Point out each Plasmodium parasite.
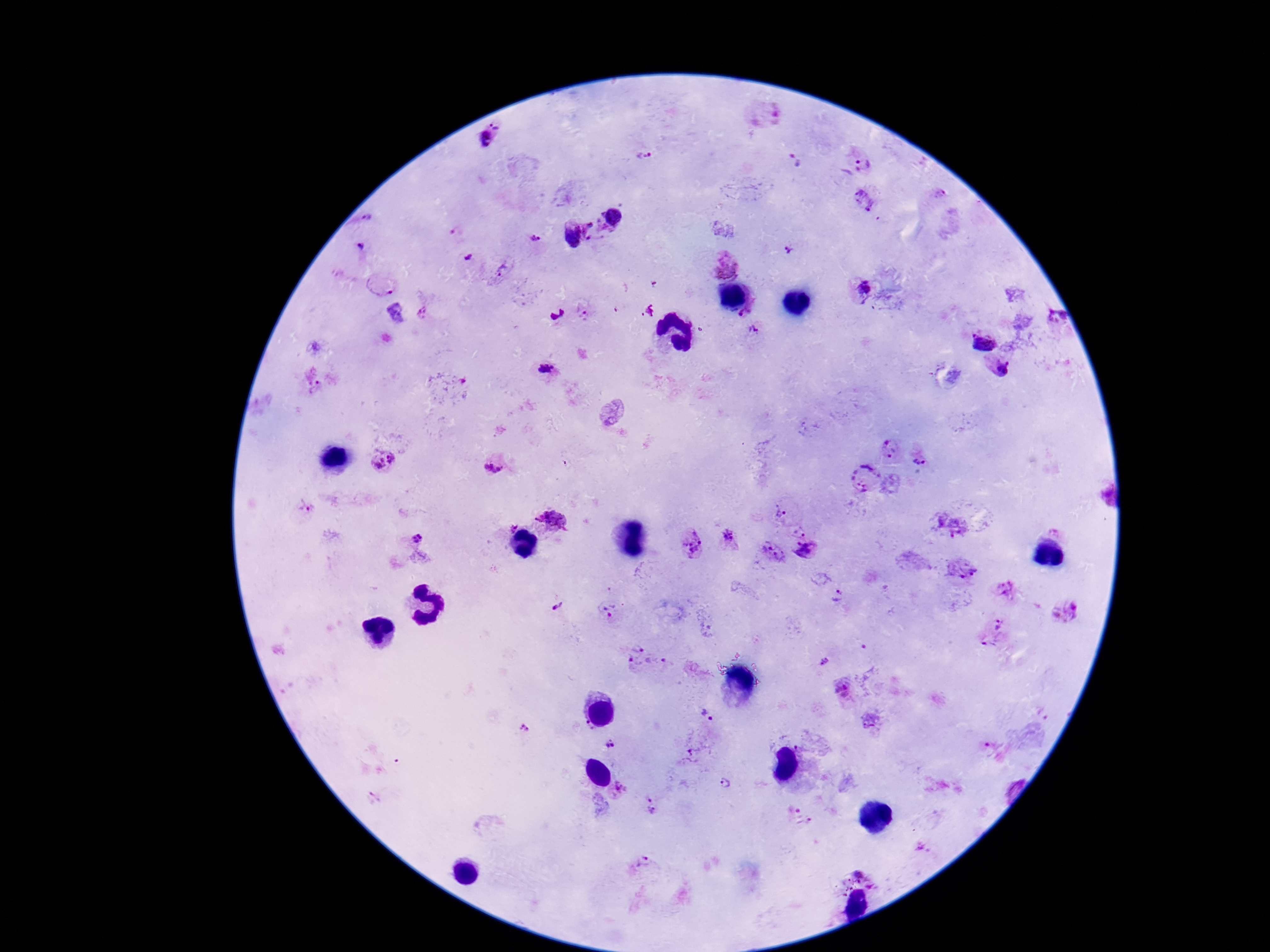

Approximate centers as (x, y) in pixels.
Plasmodium parasites: (488, 139), (641, 156), (794, 160), (855, 164), (939, 196), (866, 198), (616, 215), (596, 227), (573, 237), (534, 241), (361, 247), (787, 250), (466, 258), (723, 263), (501, 271), (386, 287), (862, 289), (423, 313), (743, 313), (584, 314), (1053, 320), (753, 331), (981, 340), (546, 368), (1004, 371), (313, 384), (891, 450), (920, 457), (383, 462), (494, 462), (868, 477), (306, 504), (781, 513), (553, 520), (954, 526), (512, 527), (1058, 531), (799, 532), (418, 539), (731, 541), (690, 545), (772, 550), (808, 552), (960, 571), (1004, 591), (842, 596), (558, 606), (610, 610), (1066, 611), (992, 632), (637, 646), (824, 660), (655, 663), (634, 665), (843, 691), (707, 715), (869, 722), (524, 728), (587, 729), (608, 743), (724, 784), (619, 790), (650, 808), (798, 817), (922, 847), (643, 865), (859, 873).

{
  "magnification": "100x",
  "preparation": "thick blood film",
  "field_of_view": "one from this slide",
  "patient_malaria_status": "infected",
  "stain": "Giemsa",
  "image_size": "1270×952 pixels",
  "capture": "smartphone camera through the microscope eyepiece"
}